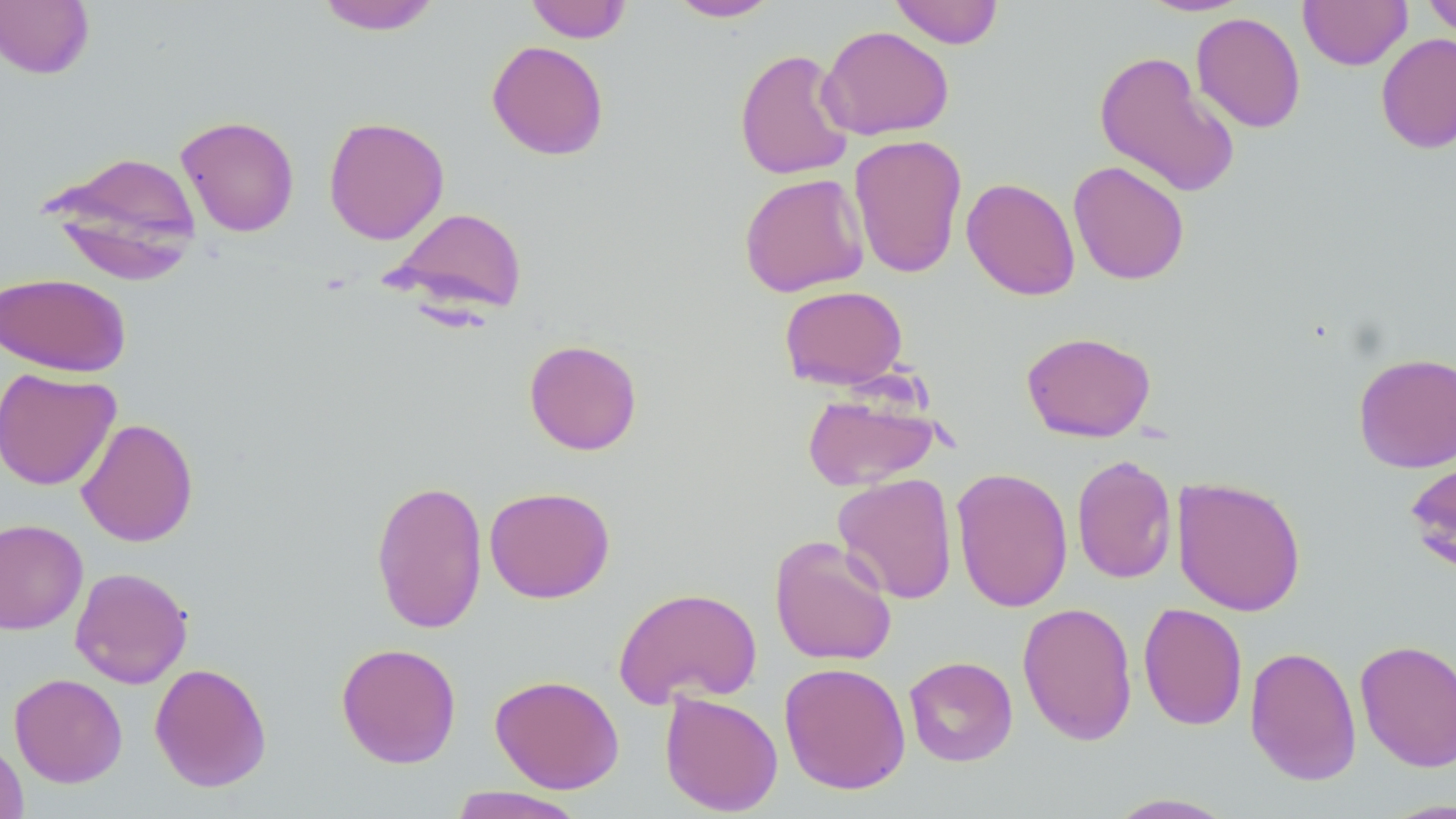 Approximate bounding boxes as (x1, y1, x2, y2) in pixels. Uninfected red blood cell locations: (0, 0, 95, 80), (314, 0, 441, 35), (525, 0, 633, 43), (668, 0, 781, 22), (889, 0, 1004, 49), (1137, 0, 1252, 16), (1299, 0, 1411, 70), (1422, 0, 1456, 40), (1190, 12, 1306, 133), (818, 24, 955, 141), (1375, 33, 1456, 154), (487, 40, 609, 160), (734, 48, 855, 180), (1094, 49, 1240, 198), (176, 115, 300, 237), (323, 116, 450, 245), (848, 134, 967, 279), (46, 150, 203, 281), (1068, 160, 1190, 285), (738, 172, 869, 297), (961, 177, 1080, 301), (386, 206, 529, 317), (0, 272, 132, 377), (779, 284, 908, 390), (1021, 331, 1156, 442), (524, 339, 642, 456), (1353, 352, 1455, 473), (0, 367, 121, 491), (802, 389, 942, 491), (76, 418, 199, 547), (1404, 452, 1456, 577), (1071, 454, 1177, 584), (951, 466, 1073, 612), (832, 472, 958, 604), (1171, 476, 1307, 616), (370, 478, 488, 635), (484, 485, 615, 603), (0, 519, 88, 634), (769, 536, 898, 667), (70, 567, 193, 688), (613, 586, 762, 709), (1017, 601, 1138, 745), (1138, 602, 1248, 731), (1354, 639, 1456, 772), (336, 642, 461, 768), (1244, 645, 1362, 786), (903, 655, 1019, 767), (779, 661, 911, 795), (149, 662, 272, 792), (9, 673, 128, 788), (489, 674, 625, 794), (659, 691, 783, 816), (0, 734, 28, 819), (447, 786, 587, 819), (1104, 793, 1240, 818). Slide-level diagnosis: negative for blood parasites. May-Grünwald-Giemsa-stained preparation. Image is 1456×819 pixels. Optical microscopy. Thin blood film. One field of a larger specimen. 1000x magnification.